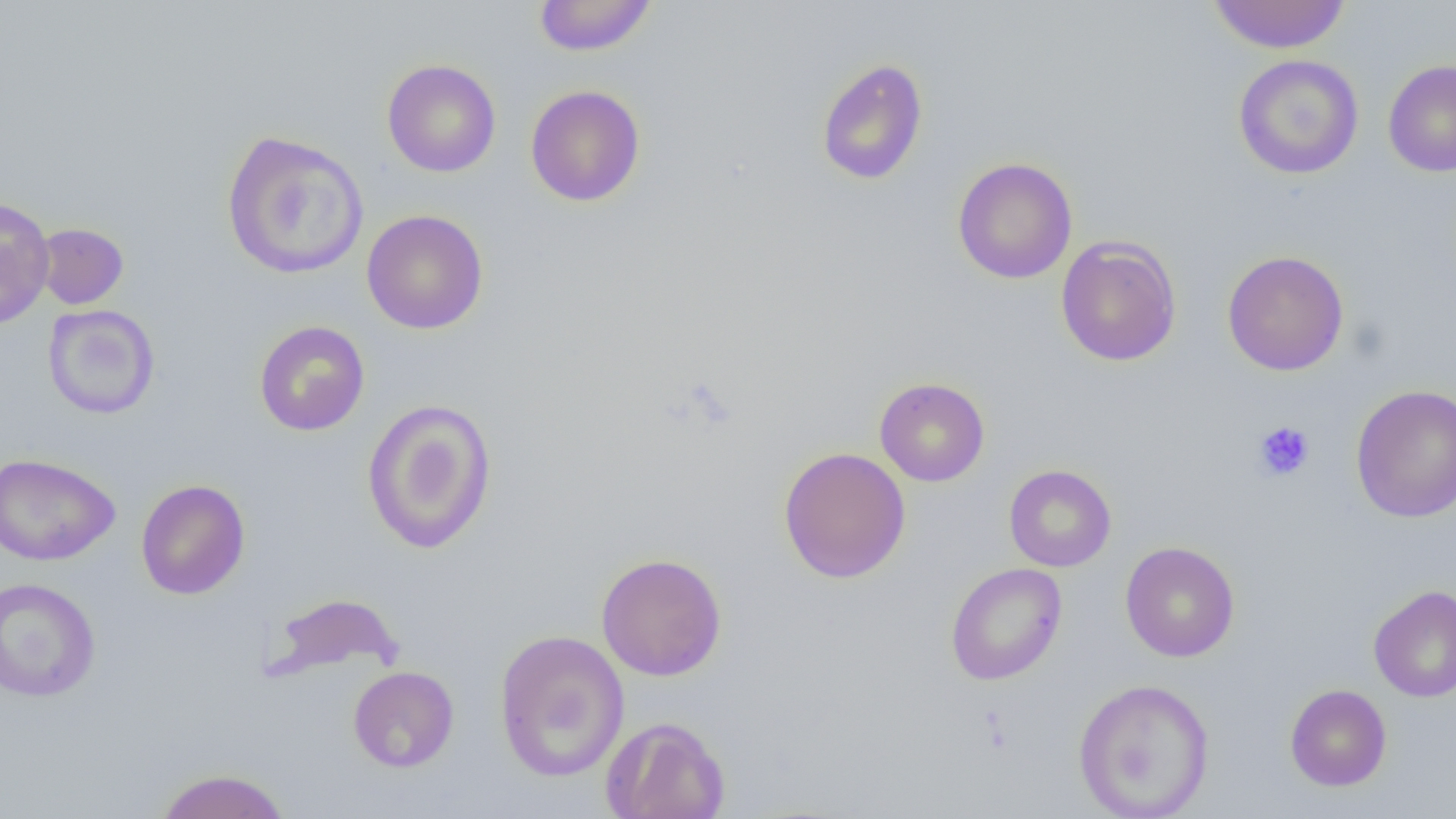
Approximate bounding boxes as [x1, y1, x2, y2] in pixels. Platelet locations: [1253, 421, 1315, 481]. Uninfected red blood cell locations: [533, 0, 657, 56], [1207, 0, 1351, 54], [1233, 54, 1364, 180], [816, 58, 928, 185], [381, 59, 501, 178], [1382, 59, 1456, 176], [524, 85, 646, 207], [221, 130, 369, 280], [952, 157, 1078, 284], [0, 197, 55, 329], [362, 210, 489, 334], [34, 222, 129, 309], [1055, 235, 1182, 367], [1222, 250, 1349, 376], [42, 304, 160, 419], [254, 320, 369, 436], [874, 377, 990, 487], [1350, 384, 1456, 523], [361, 398, 498, 555], [778, 446, 910, 584], [0, 452, 120, 566], [1004, 464, 1116, 572], [135, 479, 250, 600], [1120, 541, 1240, 662], [595, 552, 727, 681], [945, 563, 1066, 686], [0, 577, 101, 702], [1369, 585, 1456, 702], [264, 591, 405, 683], [493, 629, 630, 782], [348, 665, 459, 772], [1073, 677, 1214, 818], [1285, 684, 1392, 791], [601, 715, 730, 819], [153, 767, 292, 818]. Slide-level diagnosis: negative for blood parasites. One field of a larger specimen. Captured at 1000x magnification. Thin blood smear. Image is 1456×819 pixels. Light microscopy.